State the blood parasite species.
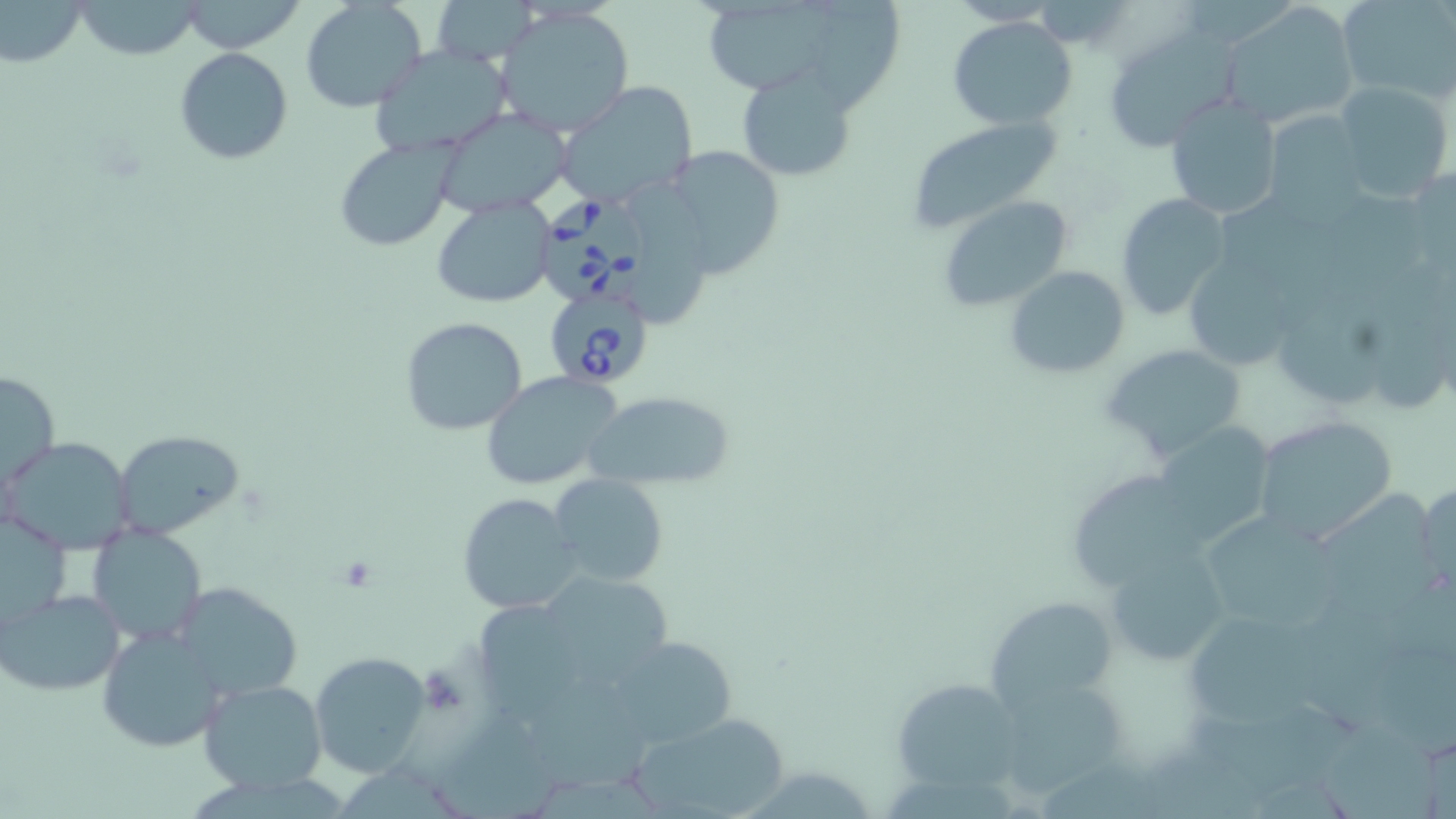
Babesia divergens.

Approximate bounding boxes as named x1/y1/x2/y2 corners in pixels. Uninfected red blood cell locations: (x1=1, y1=0, x2=90, y2=69), (x1=179, y1=0, x2=306, y2=53), (x1=430, y1=0, x2=541, y2=64), (x1=706, y1=0, x2=845, y2=87), (x1=817, y1=0, x2=903, y2=114), (x1=1336, y1=0, x2=1454, y2=103), (x1=71, y1=1, x2=204, y2=60), (x1=300, y1=1, x2=428, y2=113), (x1=1223, y1=2, x2=1363, y2=126), (x1=496, y1=6, x2=636, y2=136), (x1=946, y1=16, x2=1077, y2=129), (x1=1102, y1=28, x2=1241, y2=152), (x1=368, y1=43, x2=518, y2=157), (x1=178, y1=48, x2=296, y2=165), (x1=736, y1=67, x2=856, y2=182), (x1=555, y1=82, x2=699, y2=208), (x1=1333, y1=82, x2=1454, y2=203), (x1=1165, y1=96, x2=1282, y2=221), (x1=435, y1=109, x2=570, y2=214), (x1=1267, y1=110, x2=1367, y2=213), (x1=904, y1=115, x2=1069, y2=230), (x1=334, y1=139, x2=456, y2=250), (x1=659, y1=144, x2=787, y2=279), (x1=631, y1=177, x2=706, y2=330), (x1=1116, y1=194, x2=1232, y2=318), (x1=433, y1=196, x2=556, y2=308), (x1=939, y1=197, x2=1073, y2=310), (x1=1191, y1=262, x2=1287, y2=371), (x1=1005, y1=266, x2=1131, y2=378), (x1=401, y1=317, x2=529, y2=436), (x1=1104, y1=344, x2=1249, y2=460), (x1=1, y1=367, x2=60, y2=497), (x1=478, y1=370, x2=623, y2=490), (x1=585, y1=390, x2=736, y2=490), (x1=1251, y1=415, x2=1399, y2=545), (x1=1169, y1=422, x2=1285, y2=555), (x1=114, y1=432, x2=245, y2=537), (x1=4, y1=437, x2=135, y2=553), (x1=1078, y1=468, x2=1196, y2=588), (x1=550, y1=473, x2=669, y2=588), (x1=1416, y1=477, x2=1456, y2=597), (x1=1319, y1=487, x2=1446, y2=621), (x1=458, y1=492, x2=585, y2=615), (x1=1205, y1=506, x2=1343, y2=629), (x1=1, y1=509, x2=73, y2=631), (x1=87, y1=524, x2=209, y2=646), (x1=1107, y1=545, x2=1230, y2=665), (x1=547, y1=574, x2=676, y2=691), (x1=172, y1=582, x2=303, y2=702), (x1=0, y1=589, x2=126, y2=695), (x1=988, y1=594, x2=1117, y2=708), (x1=476, y1=599, x2=587, y2=729), (x1=1192, y1=617, x2=1329, y2=733), (x1=97, y1=626, x2=228, y2=752), (x1=606, y1=636, x2=741, y2=748), (x1=309, y1=650, x2=432, y2=775), (x1=533, y1=673, x2=658, y2=795), (x1=885, y1=676, x2=1032, y2=797), (x1=198, y1=678, x2=330, y2=792), (x1=1004, y1=683, x2=1132, y2=795), (x1=1181, y1=700, x2=1365, y2=796), (x1=434, y1=707, x2=558, y2=819), (x1=627, y1=713, x2=788, y2=817), (x1=1324, y1=713, x2=1441, y2=819). Babesia divergens-infected red blood cell locations: (x1=541, y1=193, x2=649, y2=304), (x1=543, y1=286, x2=655, y2=394). Platelet locations: (x1=335, y1=555, x2=381, y2=592). 1000x magnification. Thin blood smear. Optical microscopy. Image is 1456×819 pixels. May-Grünwald-Giemsa stain. One field of a larger specimen.